Locate every blood parasite and identify its species.
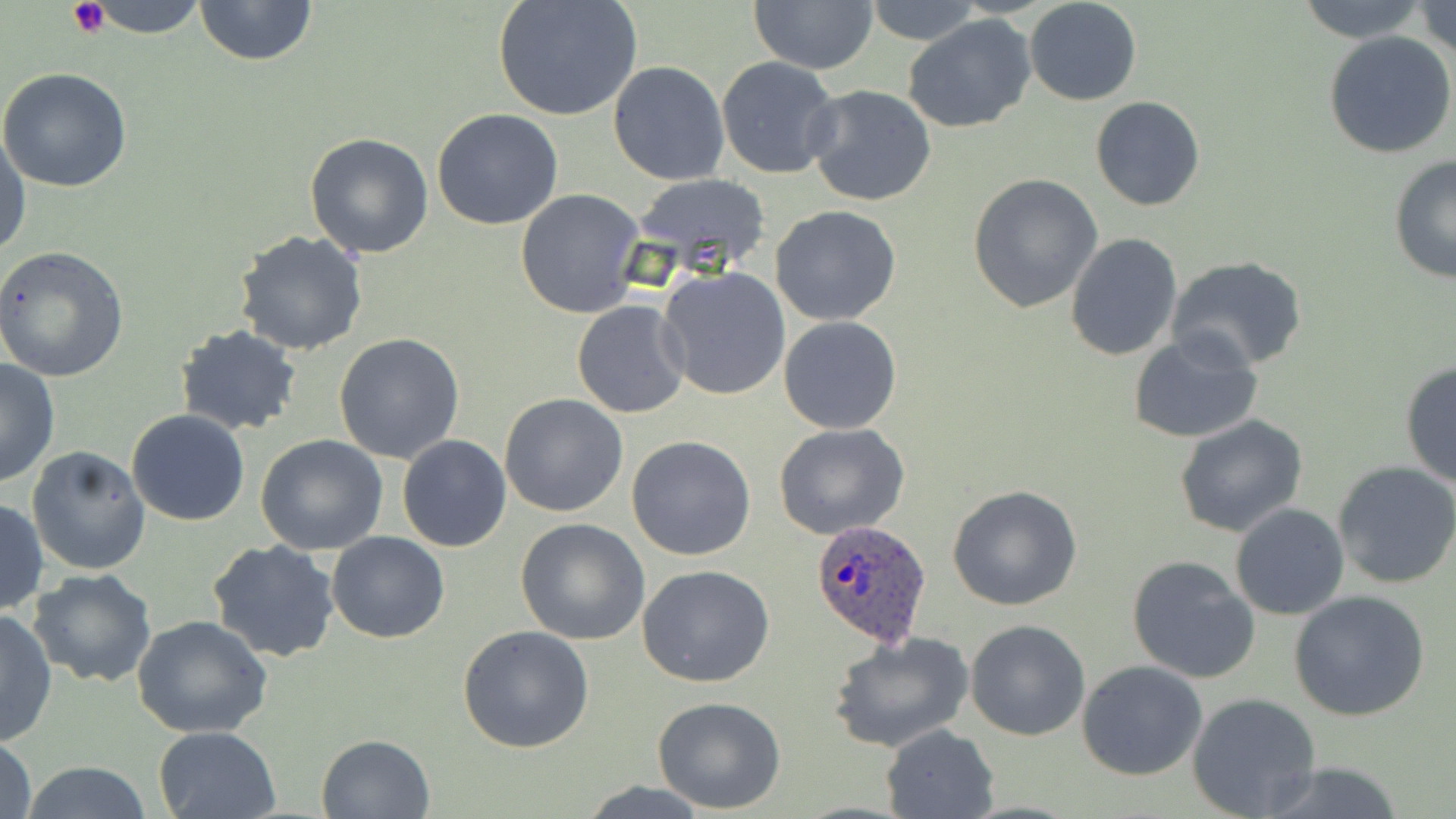

Approximate bounding boxes as named x1/y1/x2/y2 corners in pixels.
Plasmodium ovale-infected red blood cells: (x1=809, y1=518, x2=933, y2=646).
No Plasmodium falciparum, Plasmodium malariae, Plasmodium vivax, Babesia divergens, or Trypanosoma brucei observed.

slide-level diagnosis = Plasmodium ovale
uninfected red blood cell locations = approximate bounding boxes as named x1/y1/x2/y2 corners in pixels: (x1=76, y1=0, x2=212, y2=36), (x1=193, y1=0, x2=319, y2=67), (x1=492, y1=0, x2=644, y2=123), (x1=860, y1=0, x2=987, y2=45), (x1=1024, y1=0, x2=1143, y2=105), (x1=1293, y1=0, x2=1432, y2=44), (x1=1413, y1=0, x2=1456, y2=60), (x1=749, y1=1, x2=878, y2=75), (x1=903, y1=14, x2=1037, y2=133), (x1=1323, y1=31, x2=1456, y2=158), (x1=715, y1=57, x2=841, y2=178), (x1=608, y1=61, x2=729, y2=185), (x1=0, y1=68, x2=133, y2=192), (x1=803, y1=84, x2=938, y2=208), (x1=1089, y1=96, x2=1205, y2=211), (x1=431, y1=108, x2=563, y2=230), (x1=0, y1=128, x2=30, y2=260), (x1=303, y1=133, x2=434, y2=260), (x1=1388, y1=154, x2=1456, y2=285), (x1=632, y1=173, x2=771, y2=278), (x1=968, y1=173, x2=1102, y2=312), (x1=515, y1=189, x2=646, y2=320), (x1=769, y1=204, x2=901, y2=324), (x1=235, y1=229, x2=368, y2=356), (x1=1064, y1=231, x2=1183, y2=361), (x1=0, y1=245, x2=130, y2=381), (x1=1166, y1=255, x2=1312, y2=374), (x1=656, y1=265, x2=791, y2=400), (x1=572, y1=301, x2=690, y2=419), (x1=779, y1=315, x2=902, y2=433), (x1=174, y1=325, x2=303, y2=435), (x1=1126, y1=330, x2=1263, y2=445), (x1=333, y1=333, x2=465, y2=464), (x1=0, y1=358, x2=60, y2=488), (x1=1399, y1=360, x2=1455, y2=488), (x1=500, y1=393, x2=629, y2=517), (x1=126, y1=411, x2=250, y2=527), (x1=1175, y1=414, x2=1307, y2=537), (x1=773, y1=421, x2=910, y2=540), (x1=255, y1=435, x2=388, y2=555), (x1=396, y1=435, x2=512, y2=553), (x1=626, y1=435, x2=757, y2=561), (x1=26, y1=445, x2=153, y2=575), (x1=1332, y1=460, x2=1456, y2=589), (x1=947, y1=485, x2=1083, y2=611), (x1=0, y1=497, x2=49, y2=616), (x1=1229, y1=503, x2=1348, y2=620), (x1=515, y1=518, x2=650, y2=645), (x1=327, y1=531, x2=450, y2=643), (x1=208, y1=538, x2=341, y2=663), (x1=1124, y1=556, x2=1259, y2=683), (x1=637, y1=564, x2=775, y2=687), (x1=27, y1=568, x2=157, y2=687), (x1=1290, y1=591, x2=1430, y2=722), (x1=0, y1=607, x2=57, y2=747), (x1=131, y1=614, x2=273, y2=738), (x1=966, y1=619, x2=1090, y2=739), (x1=458, y1=625, x2=594, y2=753), (x1=827, y1=632, x2=975, y2=754), (x1=1077, y1=660, x2=1207, y2=781), (x1=1187, y1=693, x2=1322, y2=818), (x1=651, y1=694, x2=786, y2=812), (x1=880, y1=724, x2=1000, y2=818), (x1=152, y1=726, x2=281, y2=818), (x1=0, y1=734, x2=37, y2=819), (x1=316, y1=734, x2=436, y2=819), (x1=17, y1=761, x2=157, y2=819), (x1=1251, y1=761, x2=1412, y2=819), (x1=579, y1=781, x2=714, y2=816)
image size = 1456×819 pixels
field of view = one of a larger specimen
platelet locations = approximate bounding boxes as named x1/y1/x2/y2 corners in pixels: (x1=67, y1=0, x2=109, y2=38)
stain = May-Grünwald-Giemsa
modality = light microscopy
preparation = thin blood film
magnification = 1000x